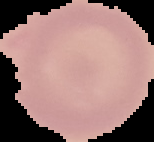
image_size: 154×142 pixels
image_type: segmented cell region on a black background
preparation: thin blood film
result: negative for malaria parasites